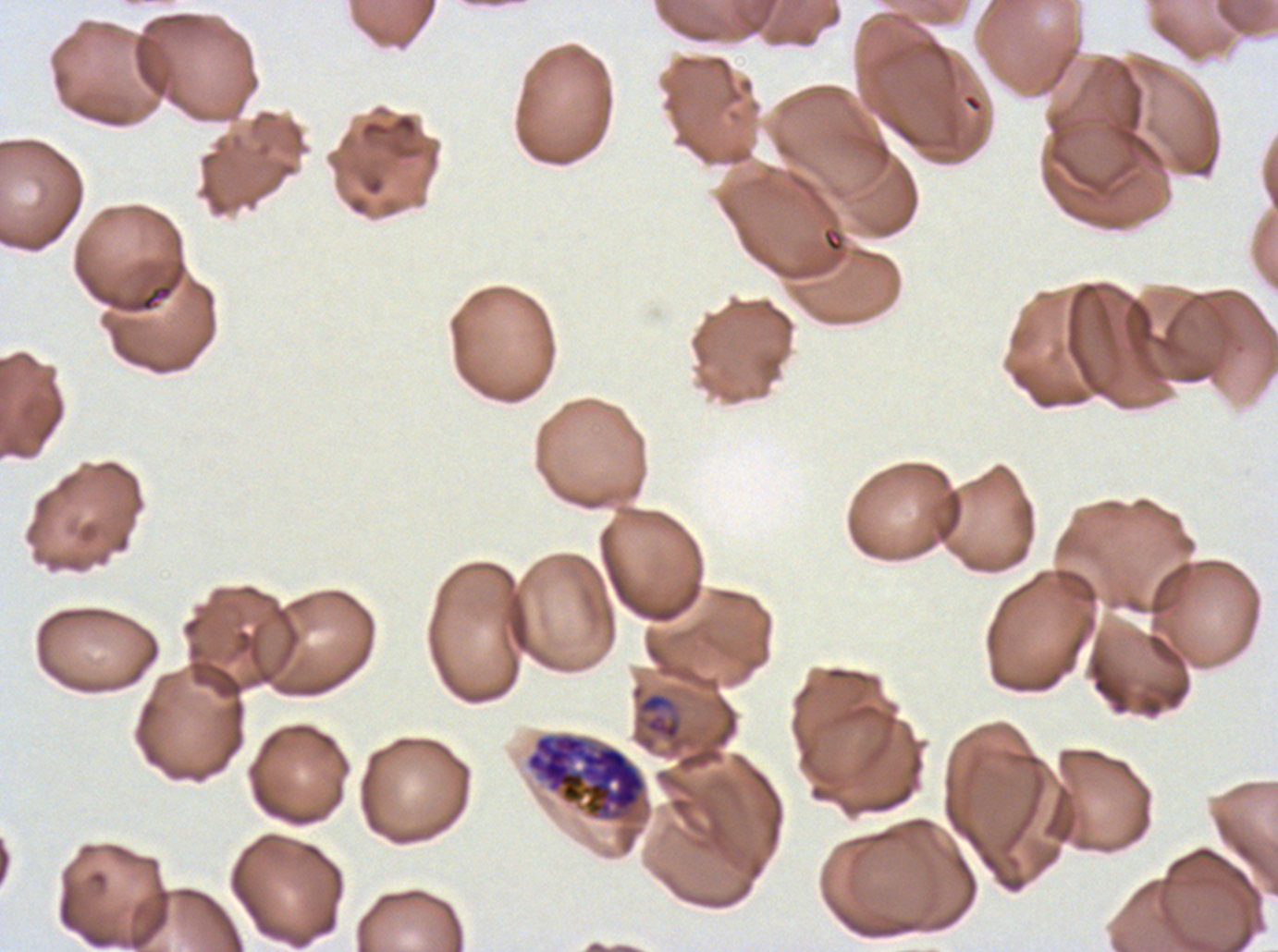 Approximate bounding boxes as (x1, y1, x2, y2) in pixels. Late schizont locations: (525, 732, 647, 822). Debris locations: (139, 284, 174, 312). Late-ring/early-trophozoite locations: (636, 691, 682, 742). Giemsa stain. Life-cycle stages observed: late-ring/early-trophozoite, late schizont. One sub-image of a larger composite. Thin blood film. Image is 1278×952 pixels. P. falciparum from a patient in The Gambia, cultured ex vivo for 24 to 48 hours.